Assess this cell for malaria.
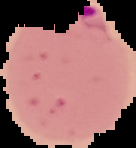

Parasitized.

Segmented cell region on a black background. Image is 136×148 pixels. From a thin blood film.